Give the extent of all uninfected red blood cells.
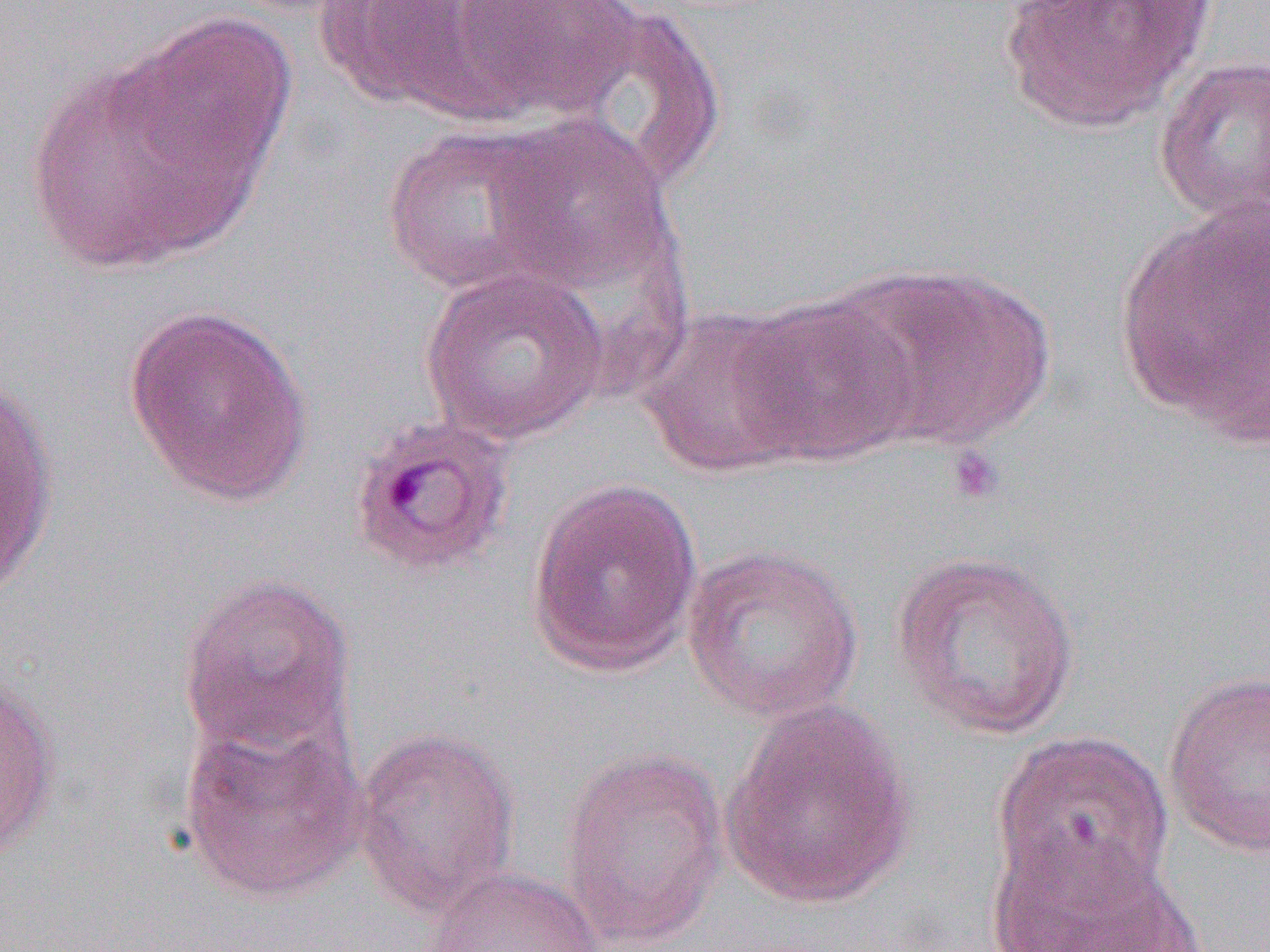
Approximate bounding boxes as [x1, y1, x2, y2] in pixels.
Uninfected red blood cells: [317, 0, 480, 111], [443, 0, 644, 122], [997, 0, 1214, 134], [541, 3, 729, 190], [21, 40, 277, 278], [1152, 55, 1270, 229], [481, 114, 682, 301], [378, 123, 568, 295], [1114, 202, 1268, 442], [831, 263, 1056, 450], [418, 266, 611, 446], [727, 292, 920, 468], [122, 302, 315, 508], [637, 305, 815, 478], [1, 376, 59, 599], [525, 477, 704, 679], [681, 543, 864, 723], [890, 549, 1082, 741], [177, 572, 355, 760], [1162, 669, 1270, 859], [0, 676, 60, 859], [719, 701, 919, 910], [176, 714, 370, 904], [351, 726, 521, 919], [992, 729, 1175, 906], [558, 747, 730, 948], [987, 832, 1194, 952], [424, 866, 602, 952].

Platelet locations: [945, 444, 1006, 507]. Slide-level diagnosis: Plasmodium ovale. One field of a larger specimen. Image is 1270×952 pixels. Captured at 1000x magnification. Thin blood film. Light microscopy.